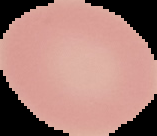

Cell region segmented out of the field of view; the surrounding area is masked to black. Image is 157×136 pixels. From a thin blood film. Result: no Plasmodium parasites seen.